Comment on the morphology of the red blood cells.
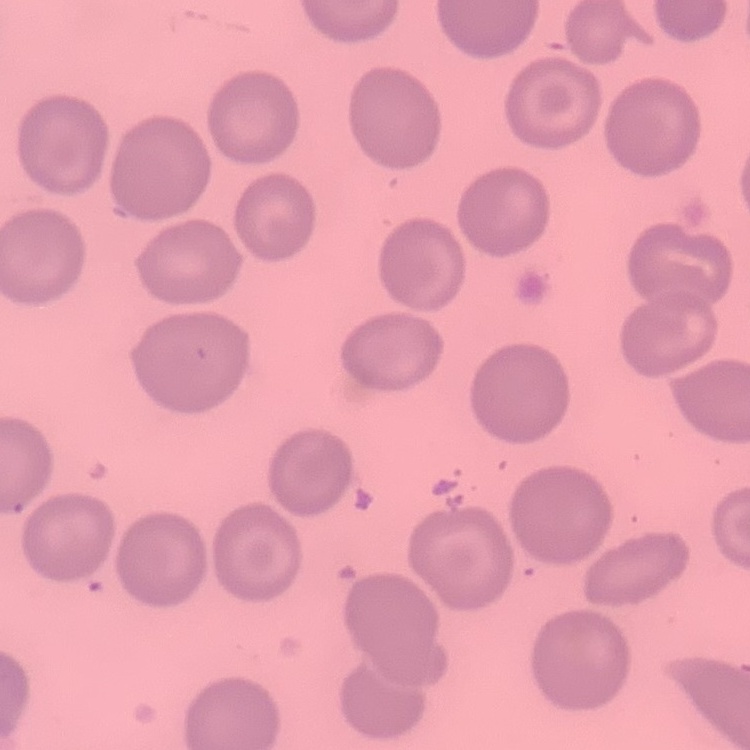

No rouleaux formation.

Summary:
  - Stain: Field's or Giemsa
  - Image type: square crop of a larger photomicrograph
  - Preparation: thin peripheral smear